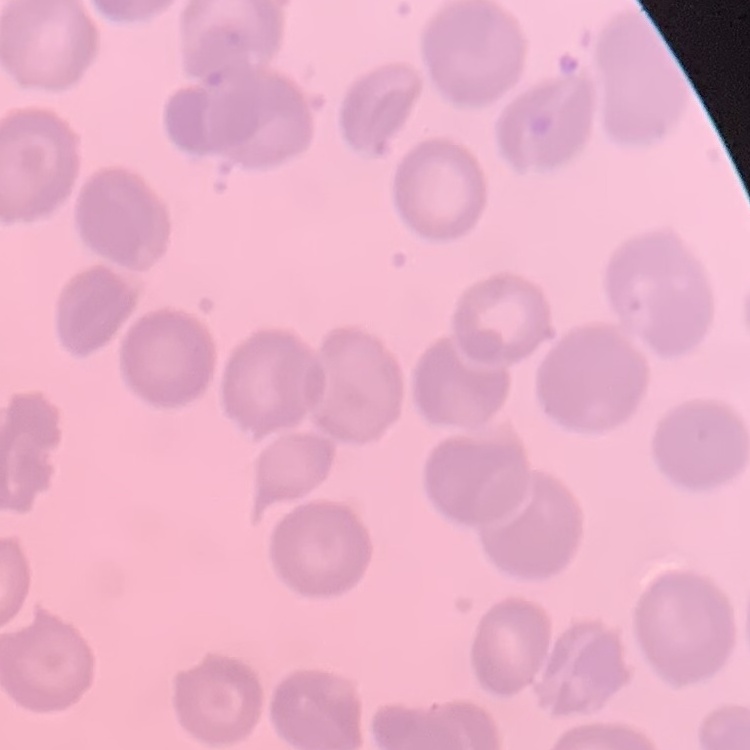 The erythrocytes show no rouleaux formation. One tile cut from a larger photomicrograph. Thin blood smear. Stained with either Field's or Giemsa.